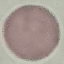

Malaria status: uninfected. Thin blood film. Acquired by smartphone through the microscope eyepiece. Giemsa stain. Automatically extracted cell patch, resized to 64 × 64 pixels.